Locate platelets.
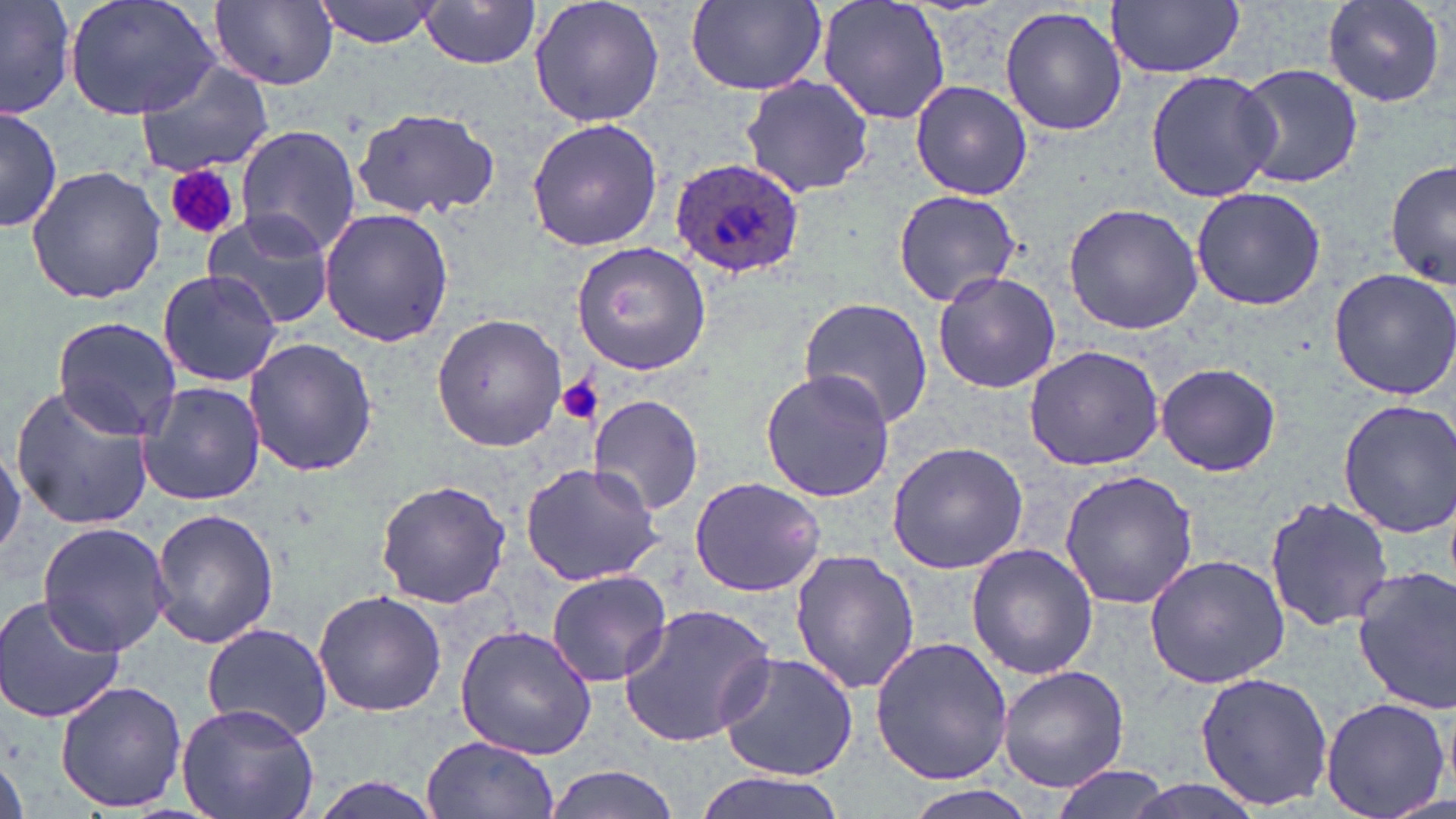
Approximate bounding boxes as (x1,y1)-(x2,y2) corner pairs in pixels.
Platelets: (165,164)-(239,241), (556,376)-(602,425).

Summary:
  - Plasmodium ovale-infected red blood cell locations: (670,157)-(806,280)
  - Uninfected red blood cell locations: (0,0)-(75,120), (63,0)-(219,122), (210,0)-(339,89), (314,0)-(442,47), (528,0)-(665,129), (684,0)-(826,97), (817,0)-(953,126), (1321,0)-(1448,109), (417,1)-(543,69), (1107,1)-(1244,78), (999,6)-(1128,137), (136,59)-(274,177), (1234,62)-(1363,189), (1144,69)-(1280,203), (737,74)-(876,198), (910,80)-(1032,201), (1,105)-(61,234), (351,108)-(503,218), (525,117)-(664,251), (234,124)-(362,254), (1386,159)-(1455,289), (25,166)-(166,305), (1191,187)-(1326,312), (893,188)-(1024,307), (1063,203)-(1204,335), (319,207)-(454,347), (201,209)-(336,329), (571,243)-(710,374), (1327,266)-(1456,399), (156,268)-(282,387), (931,271)-(1061,393), (798,297)-(935,431), (431,313)-(566,453), (51,316)-(183,440), (244,337)-(378,478), (1022,345)-(1167,471), (1156,361)-(1282,477), (760,372)-(890,502), (136,381)-(264,505), (9,384)-(157,531), (587,394)-(704,518), (1336,398)-(1456,540), (886,439)-(1029,575), (0,448)-(25,558), (519,460)-(666,586), (1058,469)-(1200,612), (688,477)-(825,598), (375,480)-(512,610), (1264,494)-(1394,632), (149,507)-(279,649), (36,521)-(173,654), (966,544)-(1099,680), (788,549)-(920,695), (1142,553)-(1290,688), (1352,567)-(1455,713), (546,569)-(673,688), (312,590)-(446,719), (0,594)-(125,725), (616,602)-(779,749), (201,622)-(333,742), (454,624)-(598,761), (869,635)-(1015,785), (715,648)-(860,781), (998,665)-(1130,792), (1195,671)-(1333,808), (55,681)-(188,811), (1320,697)-(1448,819), (176,700)-(321,819), (422,734)-(559,819), (542,765)-(684,819), (1048,765)-(1172,819), (690,772)-(856,819), (300,774)-(452,819), (1114,778)-(1270,819)
  - Slide-level diagnosis: Plasmodium ovale
  - Image size: 1456×819 pixels
  - Magnification: 1000x
  - Modality: light microscopy
  - Preparation: thin blood film
  - Field of view: one of a larger specimen
  - Stain: May-Grünwald-Giemsa